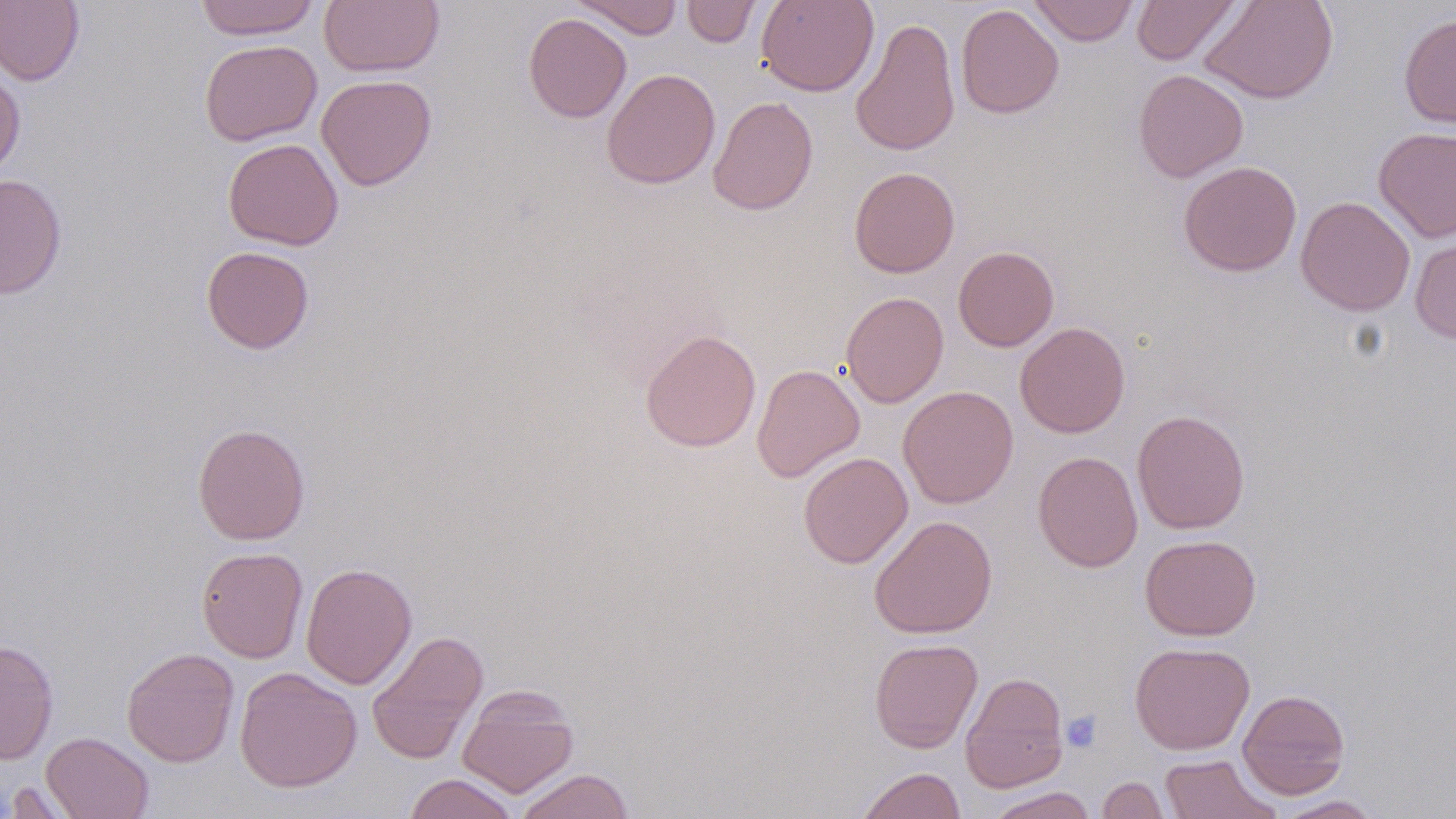 Approximate bounding boxes as (x1,y1)-(x2,y2) corner pairs in pixels. Platelet locations: (1060,709)-(1103,752). Uninfected red blood cell locations: (0,0)-(85,86), (192,0)-(321,40), (319,0)-(444,77), (571,0)-(684,39), (681,0)-(761,48), (756,0)-(879,97), (1029,0)-(1139,46), (1132,0)-(1240,65), (1200,0)-(1339,104), (955,4)-(1064,119), (524,13)-(632,123), (1398,13)-(1456,128), (850,16)-(961,157), (199,39)-(322,146), (0,66)-(26,180), (601,68)-(721,189), (1133,69)-(1249,182), (317,74)-(437,191), (708,96)-(819,215), (1373,126)-(1456,242), (222,138)-(344,251), (1178,160)-(1302,277), (849,166)-(960,278), (0,174)-(67,300), (1295,196)-(1416,316), (1409,232)-(1456,344), (953,245)-(1059,351), (201,246)-(315,354), (840,291)-(949,408), (1015,322)-(1130,438), (640,328)-(761,453), (751,364)-(865,482), (897,385)-(1018,508), (1132,409)-(1250,534), (192,423)-(310,545), (1033,450)-(1142,572), (797,451)-(913,568), (869,515)-(998,639), (1140,534)-(1261,641), (197,547)-(308,663), (301,562)-(417,689), (366,629)-(489,765), (0,638)-(59,765), (869,638)-(983,753), (1129,641)-(1255,755), (121,648)-(239,767), (234,666)-(362,793), (960,672)-(1069,792), (457,687)-(579,798), (1237,688)-(1350,799), (42,732)-(154,818), (1159,754)-(1280,818), (857,767)-(966,819), (514,769)-(635,819), (404,773)-(518,819), (1096,776)-(1172,819), (2,779)-(85,818), (985,787)-(1097,818), (1272,795)-(1384,818). Slide-level diagnosis: negative for blood parasites. Optical microscopy. One field of a larger specimen. Captured at 1000x magnification. May-Grünwald-Giemsa stain. Image is 1456×819 pixels. Thin blood film.